Locate every Plasmodium parasite.
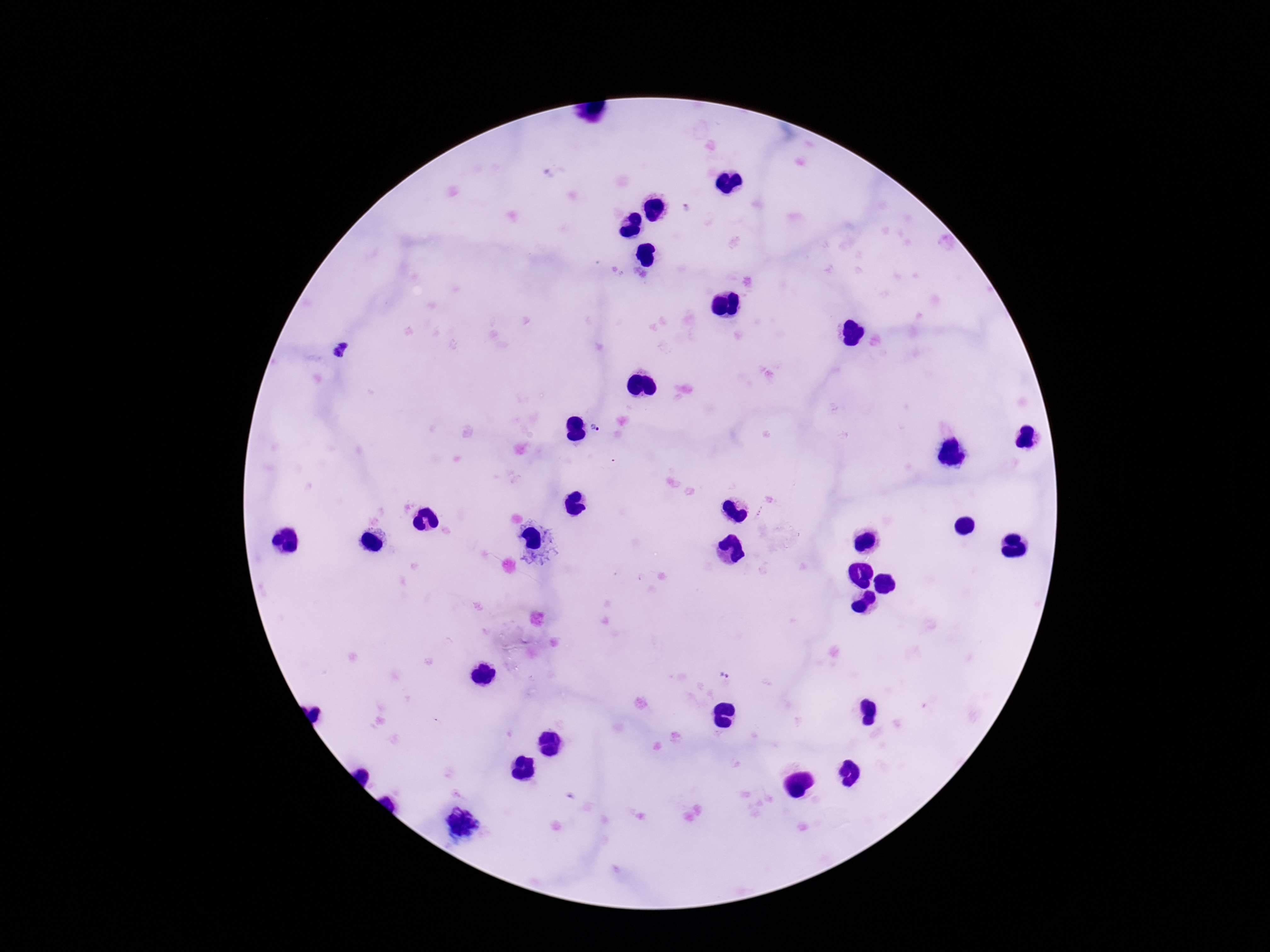
Approximate centers as {x, y} in pixels.
Plasmodium parasites: {595, 428}, {724, 675}.

field of view = single
capture = smartphone camera through the microscope eyepiece
magnification = 100x
image size = 1270×952 pixels
preparation = thick blood film
patient malaria status = infected
stain = Giemsa